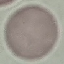 Malaria status: uninfected. Giemsa stain. Thin blood film. Photographed with a smartphone camera at the microscope eyepiece. Cell patch, automatically extracted from a larger field of view and resized to 64 × 64 pixels.